Comment on the morphology of the red blood cells.
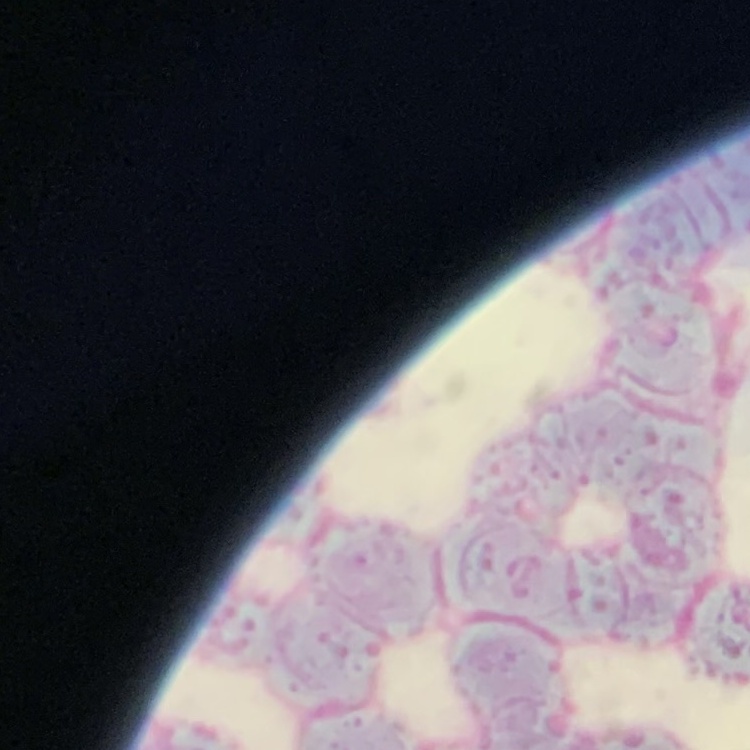
They show rouleaux formation.

Thin blood smear. Square crop of a larger photomicrograph. Field's or Giemsa stain.